Comment on the morphology of the red blood cells.
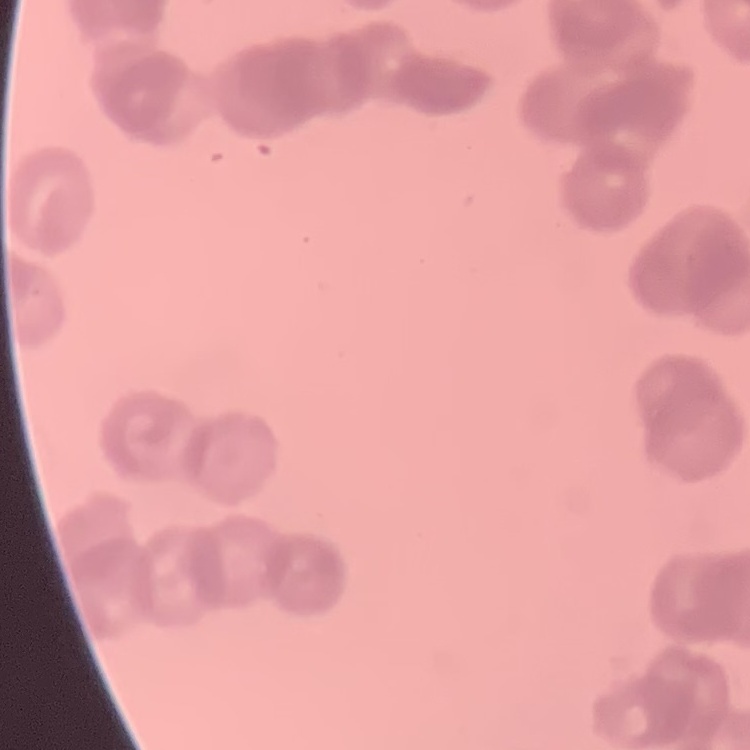

They show rouleaux formation.

Summary:
  - Image type: square crop of a larger photomicrograph
  - Preparation: thin blood smear
  - Stain: Field's or Giemsa